Assess this cell for malaria.
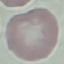
Uninfected.

Thin smear of blood. Cell patch, automatically extracted from a larger field of view and resized to 64 × 64 pixels. Giemsa stain. Acquired by smartphone through the microscope eyepiece.